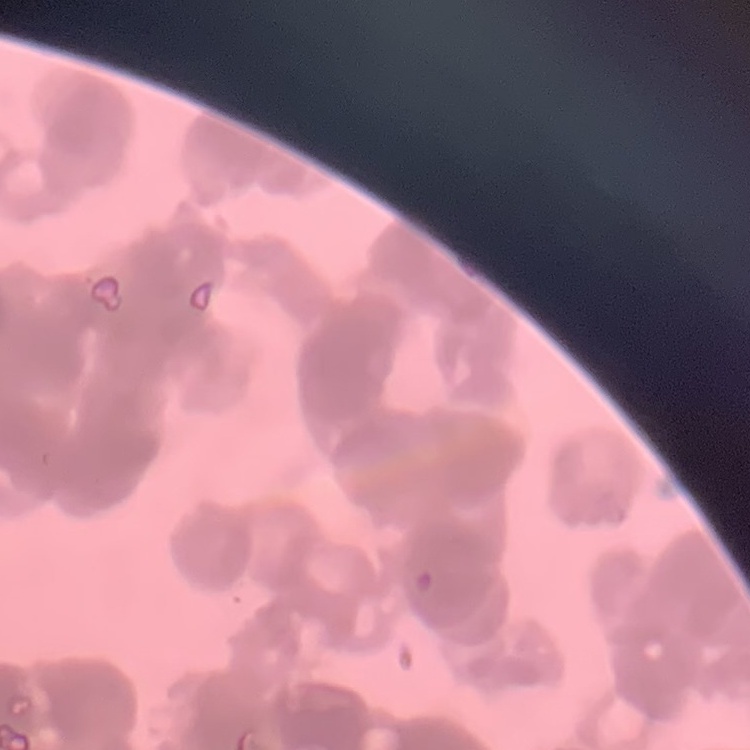 The red blood cells exhibit rouleaux formation. Stained with either Field's or Giemsa. One tile cut from a larger photomicrograph. Thin blood smear.